Outline each blood parasite and name the species.
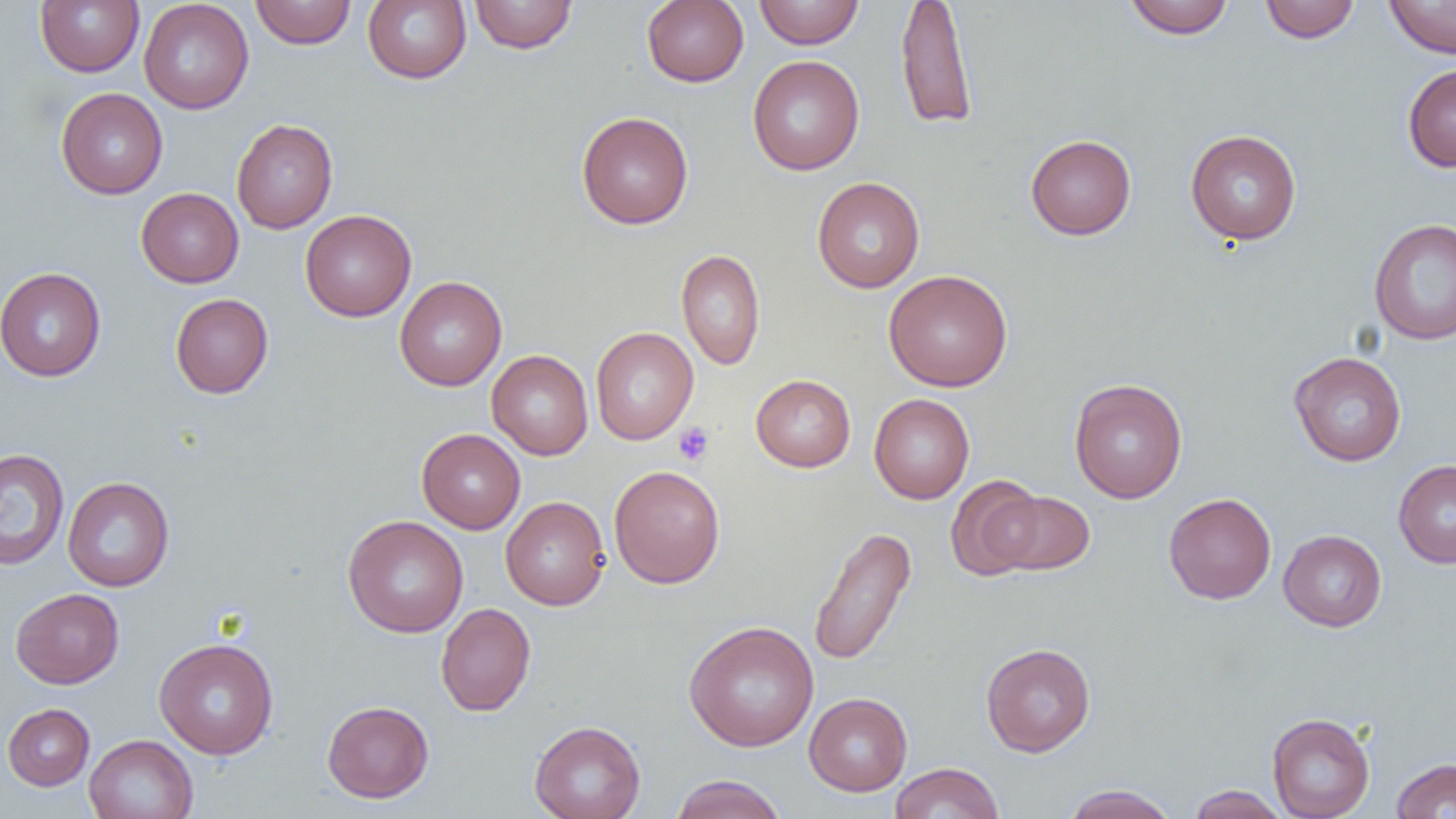
No blood parasites seen.

slide-level diagnosis = no evidence of blood parasites
image size = 1456×819 pixels
uninfected red blood cell locations = approximate bounding boxes as [x1, y1, x2, y2] in pixels: [35, 0, 144, 76], [139, 0, 254, 114], [250, 0, 356, 49], [363, 0, 471, 84], [365, 0, 577, 64], [468, 0, 577, 54], [641, 0, 749, 87], [754, 0, 865, 49], [895, 0, 977, 130], [1122, 0, 1235, 39], [1258, 0, 1361, 43], [1384, 0, 1456, 58], [748, 55, 864, 175], [1402, 63, 1456, 172], [55, 87, 168, 199], [576, 111, 694, 229], [232, 119, 338, 233], [1186, 129, 1301, 245], [1025, 134, 1136, 240], [812, 176, 925, 293], [136, 188, 244, 288], [300, 209, 416, 321], [1368, 218, 1456, 345], [676, 249, 766, 370], [0, 266, 106, 382], [884, 269, 1012, 392], [395, 276, 507, 391], [170, 293, 273, 398], [590, 327, 698, 444], [487, 350, 593, 460], [1289, 351, 1406, 466], [751, 374, 855, 472], [1069, 378, 1187, 504], [869, 394, 974, 504], [417, 428, 526, 533], [0, 448, 70, 571], [1393, 460, 1456, 568], [608, 465, 725, 588], [945, 475, 1046, 579], [62, 476, 175, 591], [991, 490, 1095, 576], [1164, 492, 1276, 604], [500, 496, 610, 610], [342, 515, 469, 637], [807, 525, 917, 666], [1278, 529, 1387, 632], [11, 588, 124, 688], [435, 603, 536, 717], [683, 620, 819, 752], [154, 637, 278, 759], [981, 642, 1095, 757], [804, 692, 913, 796], [322, 700, 434, 803], [2, 703, 94, 791], [1267, 712, 1375, 818], [530, 720, 646, 819], [84, 734, 198, 819], [1390, 758, 1456, 818], [889, 762, 1004, 819], [669, 774, 787, 819], [1062, 784, 1180, 819], [1187, 784, 1289, 818]
preparation = thin blood film
platelet locations = approximate bounding boxes as [x1, y1, x2, y2] in pixels: [673, 422, 714, 466]
field of view = single
magnification = 1000x
modality = optical microscopy